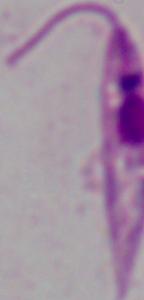
Summary:
  - Identification: Leishmania
  - Modality: photomicrograph
  - Magnification: 1000x